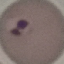
Summary:
  - Malaria status: parasitized
  - Preparation: thin smear
  - Stain: Giemsa
  - Image type: automatically extracted cell patch, resized to 64 × 64 pixels
  - Capture: smartphone camera at the microscope eyepiece